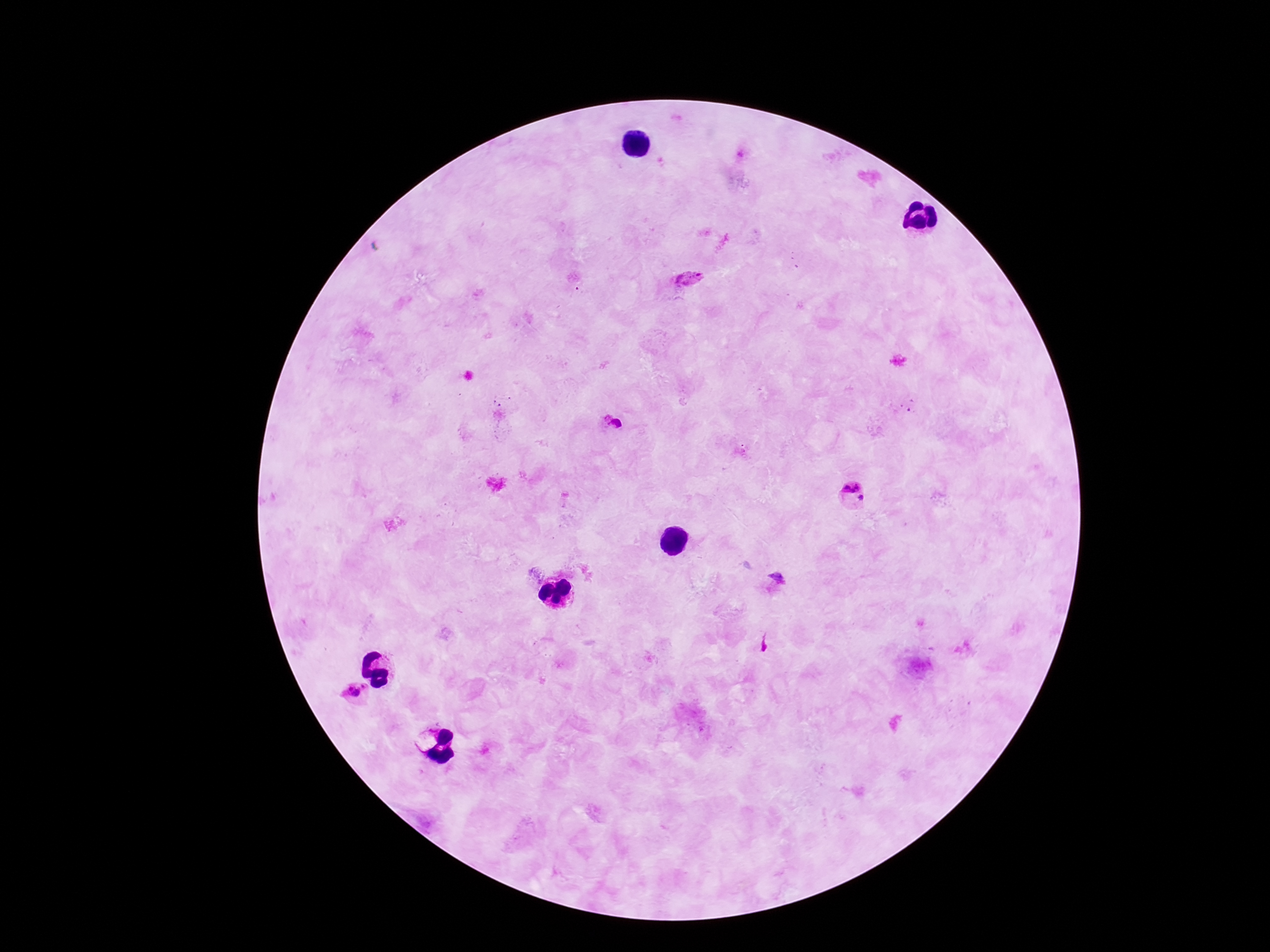

Approximate centers as [x, y] in pixels. Plasmodium parasite locations: [688, 276], [614, 420], [851, 485], [862, 498], [353, 692]. Single field of view. Thick peripheral-blood smear. Smartphone photograph taken through the microscope eyepiece. Image is 1270×952 pixels. Patient malaria status: infected. Giemsa stain. 100x magnification.